Assess this cell for malaria.
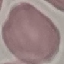

Uninfected.

Summary:
  - Preparation: thin blood smear
  - Capture: smartphone through the microscope eyepiece
  - Image type: automatically extracted cell patch, resized to 64 × 64 pixels
  - Stain: Giemsa